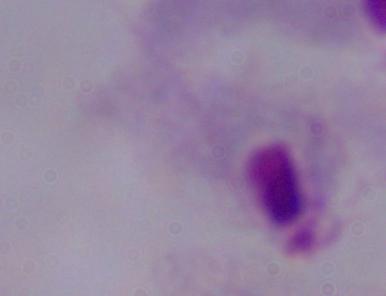

identification = trichomonad
magnification = 1000x
modality = photomicrograph